Outline each blood parasite and name the species.
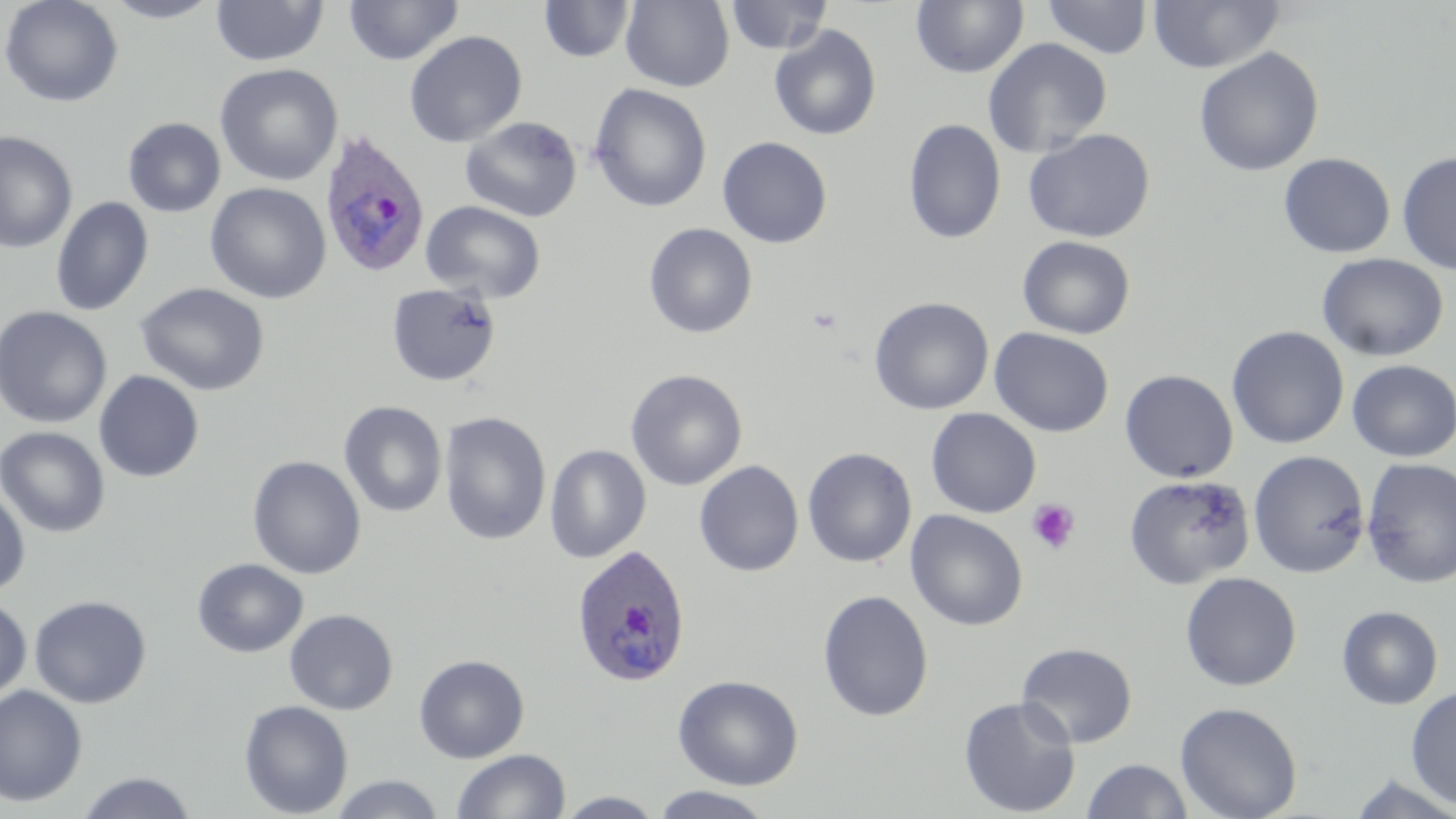

Approximate bounding boxes as (x1, y1, x2, y2) in pixels.
Plasmodium ovale-infected red blood cells: (318, 130, 431, 279), (570, 543, 692, 687).
No Plasmodium falciparum, Plasmodium malariae, Plasmodium vivax, Babesia divergens, or Trypanosoma brucei observed.

slide-level diagnosis = Plasmodium ovale
field of view = single
modality = light microscopy
image size = 1456×819 pixels
magnification = 1000x
uninfected red blood cell locations = approximate bounding boxes as (x1, y1, x2, y2) in pixels: (1, 0, 124, 108), (101, 0, 224, 23), (343, 0, 464, 66), (621, 0, 734, 92), (724, 0, 833, 55), (1041, 0, 1153, 59), (1148, 0, 1285, 74), (211, 1, 328, 66), (538, 1, 635, 63), (911, 1, 1028, 79), (769, 25, 882, 141), (404, 30, 527, 148), (982, 37, 1113, 159), (1193, 46, 1324, 177), (215, 63, 343, 186), (589, 83, 712, 213), (460, 116, 583, 222), (122, 117, 226, 217), (903, 119, 1006, 244), (1023, 128, 1156, 243), (0, 131, 78, 254), (717, 136, 832, 248), (1397, 150, 1456, 276), (1279, 153, 1395, 258), (204, 182, 331, 304), (50, 198, 154, 317), (420, 200, 546, 304), (643, 223, 758, 339), (1017, 235, 1136, 340), (1316, 252, 1449, 362), (134, 282, 270, 396), (386, 282, 501, 387), (869, 296, 993, 415), (0, 306, 112, 429), (1226, 326, 1349, 449), (989, 327, 1114, 438), (1346, 359, 1456, 462), (625, 369, 747, 491), (1120, 369, 1238, 483), (93, 370, 205, 483), (338, 401, 448, 518), (925, 408, 1041, 518), (439, 411, 552, 546), (0, 426, 110, 538), (544, 445, 651, 563), (802, 447, 917, 568), (1248, 450, 1371, 578), (247, 455, 366, 579), (1361, 457, 1456, 588), (694, 460, 804, 577), (1124, 474, 1255, 588), (0, 483, 31, 597), (905, 509, 1029, 632), (192, 558, 308, 658), (1179, 572, 1302, 691), (817, 589, 934, 722), (29, 594, 152, 708), (0, 597, 32, 703), (1336, 605, 1443, 710), (284, 609, 398, 715), (1016, 642, 1137, 748), (413, 654, 530, 763), (673, 674, 803, 790), (0, 685, 88, 807), (1406, 687, 1456, 809), (958, 695, 1080, 817), (239, 699, 354, 818), (1175, 701, 1302, 819), (452, 749, 570, 818), (1081, 758, 1193, 818), (74, 771, 198, 818), (1346, 772, 1456, 818), (329, 774, 446, 818), (649, 786, 776, 819), (554, 791, 668, 818)
platelet locations = approximate bounding boxes as (x1, y1, x2, y2) in pixels: (1026, 499, 1081, 554)
preparation = thin blood film
stain = May-Grünwald-Giemsa